Comment on the morphology of the erythrocytes.
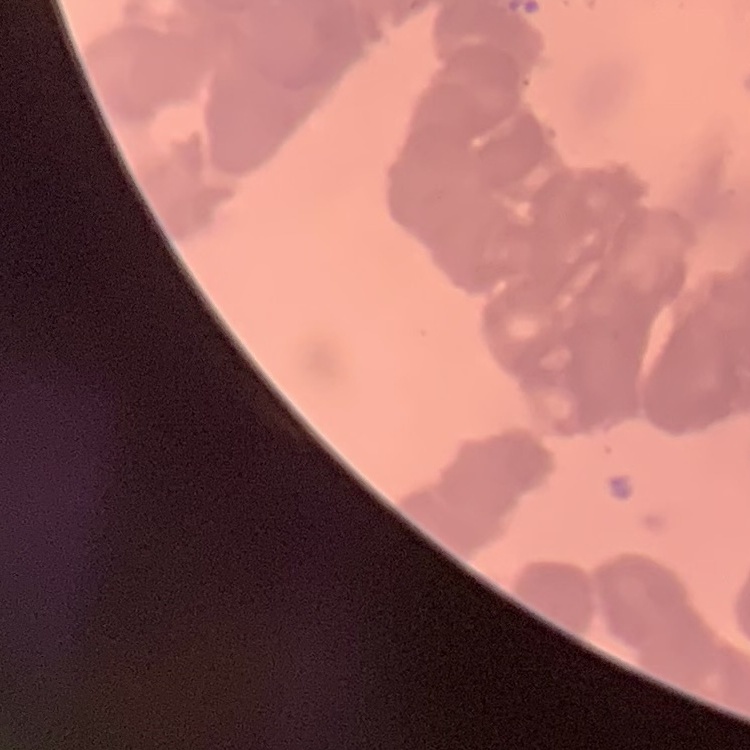

They show rouleaux formation.

Stained with either Field's or Giemsa. Square crop of a larger photomicrograph. Thin blood film.